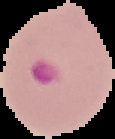

image size = 115×139 pixels
preparation = thin blood smear
image type = cell region segmented out of the field of view; surrounding area masked to black
result = malaria parasites identified